Locate and identify every blood parasite.
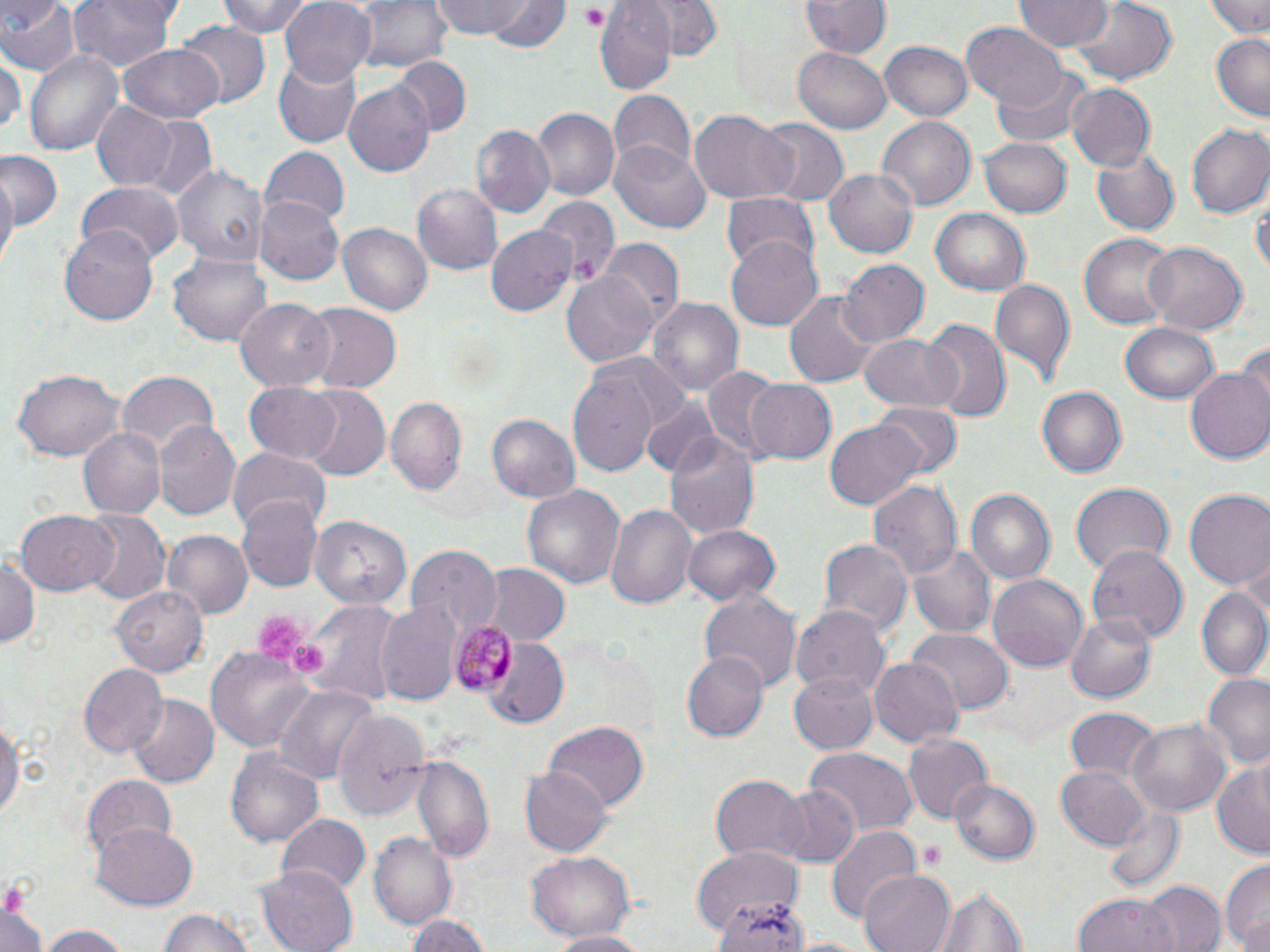

Approximate bounding boxes as named x1/y1/x2/y2 corners in pixels.
Plasmodium malariae-infected red blood cells: (x1=449, y1=619, x2=517, y2=696).
No Plasmodium falciparum, Plasmodium ovale, Plasmodium vivax, Babesia divergens, or Trypanosoma brucei observed.

Uninfected red blood cell locations: (x1=0, y1=0, x2=79, y2=76), (x1=64, y1=0, x2=180, y2=74), (x1=215, y1=0, x2=314, y2=37), (x1=279, y1=0, x2=376, y2=85), (x1=352, y1=0, x2=451, y2=73), (x1=432, y1=0, x2=540, y2=42), (x1=487, y1=0, x2=569, y2=55), (x1=648, y1=0, x2=721, y2=61), (x1=1202, y1=0, x2=1270, y2=37), (x1=598, y1=1, x2=676, y2=91), (x1=801, y1=1, x2=890, y2=60), (x1=1014, y1=1, x2=1113, y2=53), (x1=1069, y1=1, x2=1175, y2=87), (x1=962, y1=22, x2=1066, y2=109), (x1=178, y1=23, x2=270, y2=108), (x1=1212, y1=31, x2=1270, y2=120), (x1=879, y1=38, x2=975, y2=121), (x1=120, y1=41, x2=225, y2=123), (x1=793, y1=47, x2=892, y2=133), (x1=24, y1=48, x2=125, y2=158), (x1=0, y1=56, x2=24, y2=142), (x1=274, y1=56, x2=363, y2=148), (x1=397, y1=56, x2=471, y2=133), (x1=991, y1=66, x2=1091, y2=150), (x1=344, y1=83, x2=434, y2=178), (x1=1064, y1=83, x2=1154, y2=173), (x1=610, y1=91, x2=696, y2=178), (x1=92, y1=103, x2=176, y2=190), (x1=531, y1=108, x2=619, y2=201), (x1=690, y1=111, x2=797, y2=205), (x1=133, y1=117, x2=218, y2=200), (x1=877, y1=117, x2=975, y2=212), (x1=756, y1=121, x2=848, y2=206), (x1=471, y1=123, x2=555, y2=217), (x1=1186, y1=124, x2=1270, y2=218), (x1=979, y1=135, x2=1072, y2=218), (x1=610, y1=143, x2=710, y2=233), (x1=1090, y1=145, x2=1179, y2=236), (x1=260, y1=146, x2=350, y2=226), (x1=0, y1=153, x2=64, y2=228), (x1=171, y1=162, x2=269, y2=267), (x1=0, y1=167, x2=19, y2=270), (x1=827, y1=167, x2=921, y2=259), (x1=75, y1=181, x2=183, y2=264), (x1=411, y1=182, x2=503, y2=276), (x1=721, y1=192, x2=820, y2=271), (x1=1253, y1=194, x2=1269, y2=281), (x1=255, y1=195, x2=343, y2=286), (x1=535, y1=198, x2=619, y2=287), (x1=930, y1=208, x2=1031, y2=296), (x1=62, y1=222, x2=161, y2=325), (x1=337, y1=223, x2=431, y2=314), (x1=486, y1=223, x2=579, y2=314), (x1=1079, y1=232, x2=1178, y2=330), (x1=725, y1=236, x2=822, y2=332), (x1=600, y1=238, x2=684, y2=325), (x1=1142, y1=243, x2=1248, y2=334), (x1=168, y1=253, x2=271, y2=345), (x1=837, y1=258, x2=927, y2=346), (x1=562, y1=269, x2=659, y2=367), (x1=991, y1=280, x2=1076, y2=387), (x1=786, y1=292, x2=876, y2=387), (x1=645, y1=296, x2=744, y2=399), (x1=235, y1=298, x2=335, y2=391), (x1=302, y1=301, x2=402, y2=395), (x1=919, y1=321, x2=1011, y2=423), (x1=1121, y1=323, x2=1218, y2=402), (x1=860, y1=331, x2=962, y2=412), (x1=700, y1=366, x2=790, y2=459), (x1=12, y1=367, x2=128, y2=462), (x1=568, y1=367, x2=661, y2=478), (x1=1185, y1=368, x2=1270, y2=463), (x1=115, y1=370, x2=219, y2=456), (x1=744, y1=377, x2=838, y2=464), (x1=244, y1=382, x2=345, y2=463), (x1=1037, y1=386, x2=1127, y2=478), (x1=296, y1=388, x2=389, y2=480), (x1=387, y1=397, x2=468, y2=499), (x1=640, y1=399, x2=722, y2=480), (x1=869, y1=401, x2=962, y2=478), (x1=486, y1=410, x2=580, y2=504), (x1=825, y1=418, x2=925, y2=509), (x1=152, y1=420, x2=241, y2=524), (x1=77, y1=424, x2=166, y2=520), (x1=663, y1=433, x2=760, y2=540), (x1=226, y1=448, x2=330, y2=531), (x1=865, y1=478, x2=961, y2=586), (x1=1070, y1=482, x2=1173, y2=578), (x1=522, y1=483, x2=625, y2=594), (x1=963, y1=488, x2=1055, y2=587), (x1=1184, y1=489, x2=1270, y2=591), (x1=235, y1=498, x2=323, y2=593), (x1=606, y1=505, x2=695, y2=608), (x1=15, y1=509, x2=119, y2=596), (x1=82, y1=510, x2=170, y2=605), (x1=309, y1=515, x2=411, y2=611), (x1=683, y1=523, x2=780, y2=608), (x1=163, y1=530, x2=252, y2=620), (x1=818, y1=536, x2=910, y2=639), (x1=406, y1=543, x2=500, y2=637), (x1=908, y1=543, x2=999, y2=638), (x1=1086, y1=545, x2=1188, y2=645), (x1=0, y1=552, x2=41, y2=655), (x1=486, y1=563, x2=570, y2=644), (x1=988, y1=573, x2=1088, y2=673), (x1=112, y1=584, x2=212, y2=674), (x1=1196, y1=587, x2=1270, y2=679), (x1=702, y1=590, x2=801, y2=697), (x1=298, y1=598, x2=402, y2=705), (x1=376, y1=601, x2=459, y2=704), (x1=790, y1=606, x2=890, y2=697), (x1=1064, y1=610, x2=1160, y2=705), (x1=908, y1=629, x2=1011, y2=714), (x1=487, y1=639, x2=571, y2=726), (x1=205, y1=647, x2=319, y2=753), (x1=680, y1=650, x2=768, y2=741), (x1=870, y1=658, x2=960, y2=749), (x1=78, y1=663, x2=167, y2=760), (x1=788, y1=669, x2=878, y2=755), (x1=1199, y1=673, x2=1270, y2=767), (x1=270, y1=682, x2=380, y2=782), (x1=126, y1=694, x2=218, y2=786), (x1=1065, y1=707, x2=1159, y2=784), (x1=332, y1=709, x2=432, y2=821), (x1=0, y1=713, x2=22, y2=829), (x1=1131, y1=719, x2=1230, y2=817), (x1=544, y1=722, x2=649, y2=814), (x1=903, y1=732, x2=991, y2=824), (x1=803, y1=747, x2=918, y2=833), (x1=227, y1=749, x2=323, y2=845), (x1=409, y1=755, x2=493, y2=862), (x1=1210, y1=757, x2=1270, y2=857), (x1=519, y1=764, x2=612, y2=855), (x1=1057, y1=765, x2=1151, y2=851), (x1=708, y1=774, x2=811, y2=864), (x1=82, y1=776, x2=177, y2=861), (x1=949, y1=778, x2=1040, y2=864), (x1=775, y1=786, x2=860, y2=870), (x1=1102, y1=803, x2=1185, y2=896), (x1=277, y1=813, x2=370, y2=896), (x1=93, y1=821, x2=196, y2=909), (x1=825, y1=823, x2=922, y2=924), (x1=371, y1=832, x2=459, y2=930), (x1=693, y1=843, x2=805, y2=934), (x1=526, y1=852, x2=636, y2=943), (x1=1219, y1=859, x2=1270, y2=952), (x1=259, y1=863, x2=358, y2=951), (x1=857, y1=869, x2=955, y2=952), (x1=1141, y1=879, x2=1228, y2=952), (x1=707, y1=885, x2=810, y2=952), (x1=937, y1=886, x2=1032, y2=952), (x1=1073, y1=894, x2=1179, y2=952), (x1=714, y1=899, x2=814, y2=952), (x1=0, y1=901, x2=47, y2=952), (x1=160, y1=909, x2=256, y2=952), (x1=406, y1=913, x2=490, y2=952), (x1=39, y1=925, x2=134, y2=952), (x1=547, y1=931, x2=651, y2=952). Platelet locations: (x1=578, y1=4, x2=610, y2=30), (x1=252, y1=613, x2=304, y2=663), (x1=289, y1=640, x2=326, y2=676), (x1=917, y1=840, x2=949, y2=871). Slide-level diagnosis: Plasmodium malariae. May-Grünwald-Giemsa-stained preparation. Single field of view. Thin blood film. Captured at 1000x magnification. Light microscopy. Image is 1270×952 pixels.